Report the malaria status of this cell.
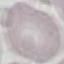

Uninfected.

capture = smartphone through the microscope eyepiece
image type = automatically extracted cell patch, resized to 64 × 64 pixels
stain = Giemsa
preparation = thin blood film